Report the malaria status of this cell.
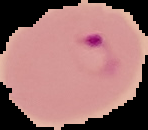
It is parasitized.

Image is 148×130 pixels. From a thin blood film. The area outside the segmented cell region is set to black.